Locate every Plasmodium falciparum-infected red blood cell.
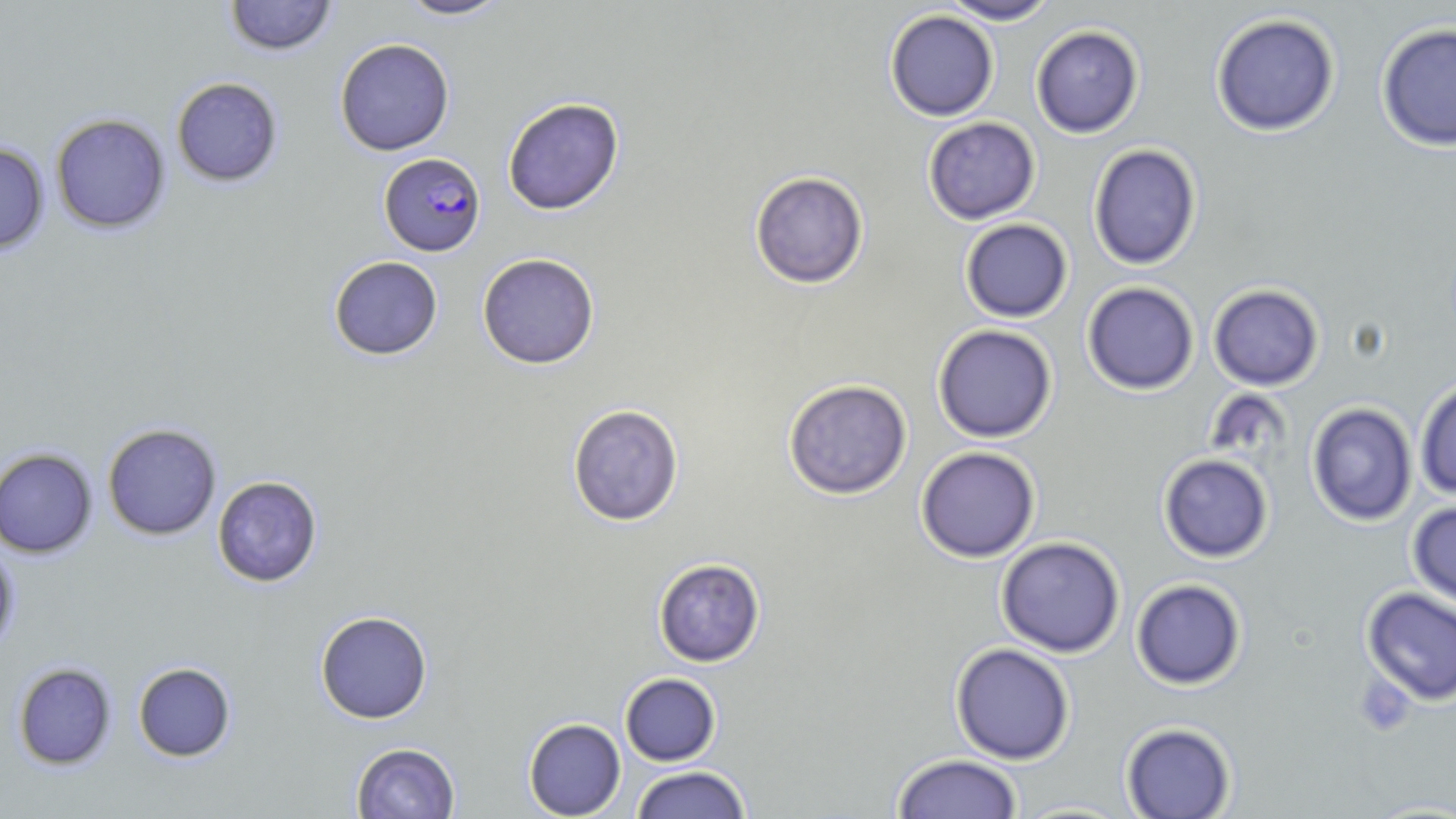

Approximate bounding boxes as (x1, y1, x2, y2) in pixels.
Plasmodium falciparum-infected red blood cells: (379, 152, 486, 256).

slide-level diagnosis = Plasmodium falciparum
image size = 1456×819 pixels
field of view = one of a larger specimen
preparation = thin blood film
stain = May-Grünwald-Giemsa
magnification = 1000x
modality = light microscopy
uninfected red blood cell locations = approximate bounding boxes as (x1, y1, x2, y2) in pixels: (224, 0, 337, 56), (396, 0, 513, 21), (940, 0, 1059, 25), (884, 10, 999, 121), (1211, 13, 1340, 136), (1376, 22, 1456, 151), (1031, 25, 1144, 138), (335, 38, 455, 156), (171, 77, 283, 187), (502, 97, 625, 215), (50, 113, 170, 234), (923, 117, 1041, 224), (0, 143, 50, 254), (1088, 143, 1202, 270), (749, 171, 869, 289), (960, 218, 1073, 322), (477, 252, 600, 369), (328, 255, 443, 360), (1082, 282, 1199, 395), (1208, 284, 1324, 391), (932, 324, 1057, 443), (1415, 378, 1456, 500), (783, 379, 912, 499), (1306, 402, 1417, 526), (567, 403, 685, 526), (102, 423, 222, 540), (916, 447, 1040, 563), (0, 448, 97, 558), (1158, 454, 1273, 562), (212, 476, 323, 587), (1407, 501, 1456, 613), (996, 537, 1125, 658), (0, 543, 20, 655), (653, 558, 765, 667), (1131, 578, 1247, 689), (1361, 587, 1456, 705), (315, 610, 433, 723), (950, 642, 1075, 765), (132, 662, 236, 762), (13, 663, 116, 769), (620, 673, 721, 766), (524, 718, 626, 818), (1121, 722, 1236, 818), (351, 742, 460, 818), (892, 753, 1024, 818), (630, 766, 752, 818), (1011, 800, 1138, 818)